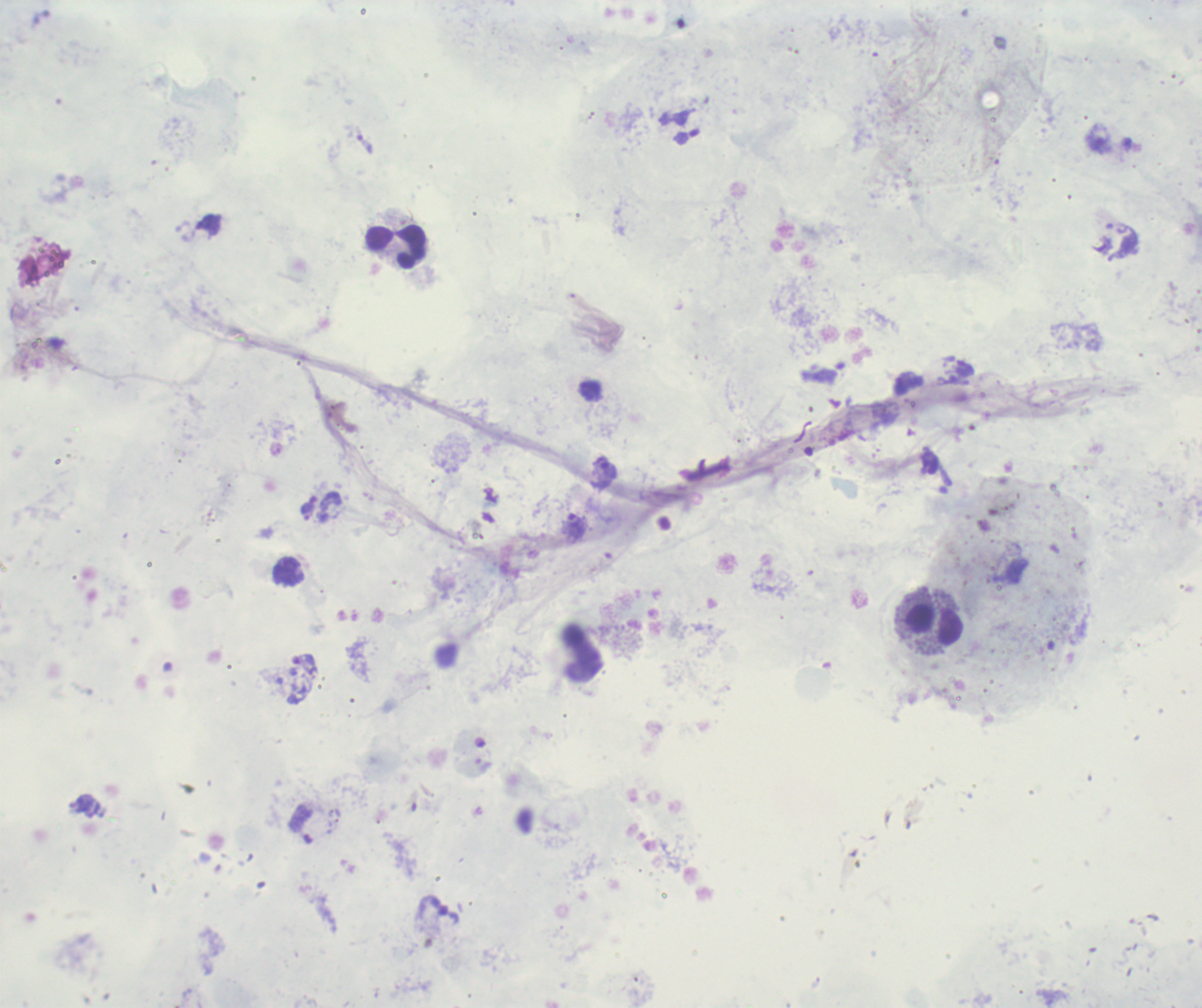 Approximate centers as [x, y] in pixels. Trophozoite locations: [364, 144], [307, 512], [575, 525]. Leukocyte locations: [395, 246], [934, 624]. Romanowsky-stained preparation. Image is 1202×1008 pixels. 100x magnification. One field from this slide. Result: positive for malaria parasites. Background quality: poor. Thick blood film. Previously used in a real diagnosis.